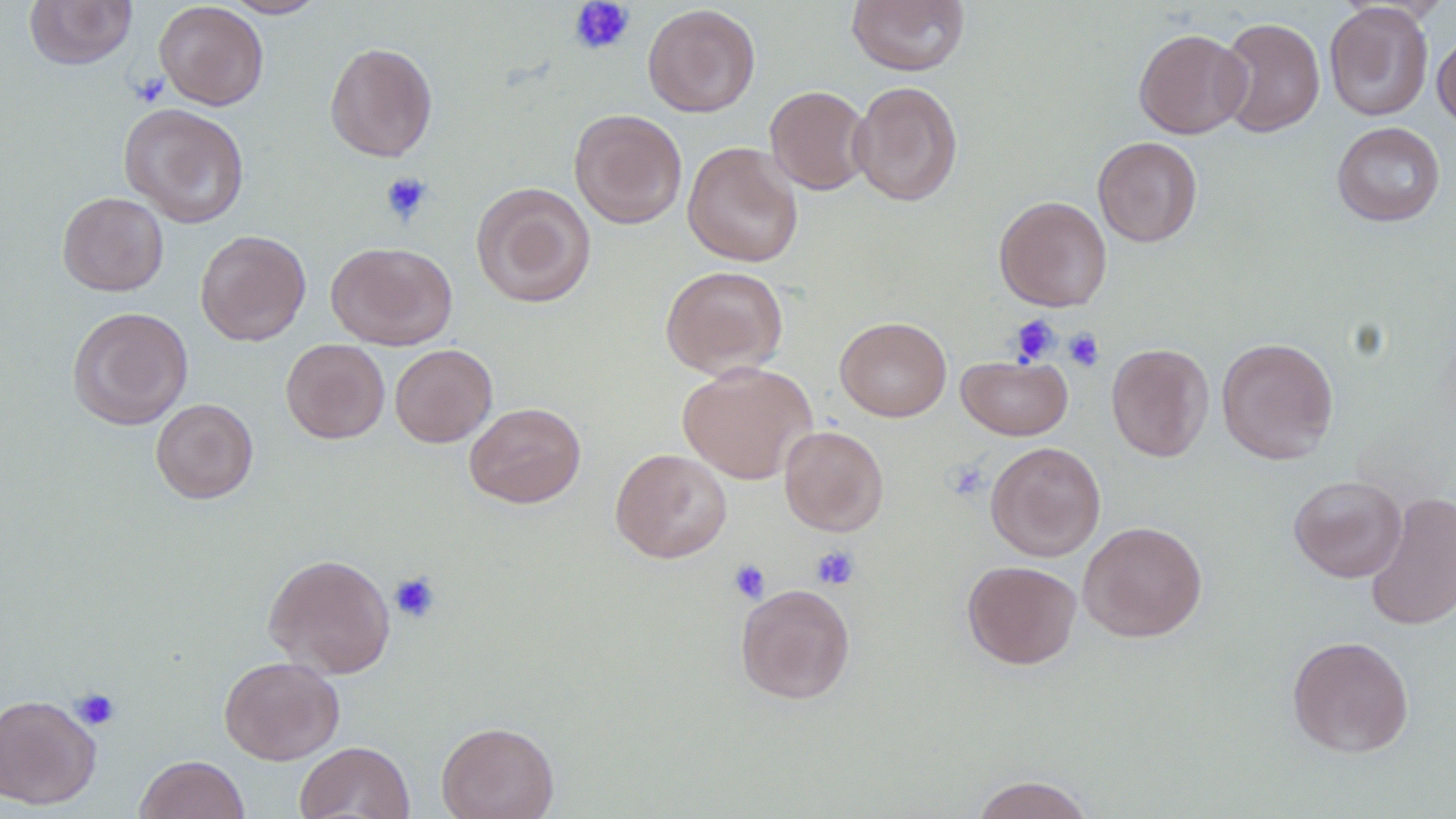 Approximate bounding boxes as named x1/y1/x2/y2 corners in pixels. Uninfected red blood cell locations: (x1=25, y1=0, x2=137, y2=70), (x1=223, y1=0, x2=328, y2=18), (x1=154, y1=1, x2=269, y2=110), (x1=847, y1=1, x2=970, y2=76), (x1=1324, y1=2, x2=1434, y2=121), (x1=642, y1=3, x2=761, y2=117), (x1=1217, y1=16, x2=1325, y2=137), (x1=1134, y1=28, x2=1252, y2=139), (x1=1432, y1=30, x2=1456, y2=133), (x1=324, y1=41, x2=438, y2=162), (x1=849, y1=80, x2=963, y2=206), (x1=765, y1=85, x2=873, y2=195), (x1=119, y1=103, x2=250, y2=228), (x1=569, y1=108, x2=687, y2=229), (x1=1331, y1=121, x2=1446, y2=227), (x1=1092, y1=136, x2=1203, y2=247), (x1=682, y1=141, x2=803, y2=268), (x1=471, y1=182, x2=597, y2=308), (x1=57, y1=191, x2=169, y2=296), (x1=994, y1=195, x2=1112, y2=312), (x1=195, y1=229, x2=311, y2=345), (x1=326, y1=241, x2=457, y2=350), (x1=660, y1=265, x2=789, y2=379), (x1=67, y1=306, x2=193, y2=430), (x1=835, y1=316, x2=952, y2=421), (x1=1216, y1=337, x2=1339, y2=464), (x1=281, y1=339, x2=390, y2=444), (x1=1106, y1=342, x2=1213, y2=461), (x1=390, y1=344, x2=497, y2=447), (x1=957, y1=355, x2=1073, y2=441), (x1=677, y1=361, x2=816, y2=484), (x1=150, y1=398, x2=259, y2=504), (x1=464, y1=402, x2=586, y2=508), (x1=779, y1=425, x2=889, y2=536), (x1=985, y1=442, x2=1106, y2=562), (x1=611, y1=448, x2=732, y2=563), (x1=1288, y1=475, x2=1407, y2=583), (x1=1364, y1=491, x2=1456, y2=631), (x1=1078, y1=521, x2=1207, y2=642), (x1=262, y1=553, x2=396, y2=678), (x1=962, y1=560, x2=1081, y2=669), (x1=735, y1=583, x2=856, y2=704), (x1=1287, y1=635, x2=1415, y2=758), (x1=218, y1=656, x2=345, y2=765), (x1=0, y1=694, x2=102, y2=810), (x1=436, y1=721, x2=559, y2=819), (x1=296, y1=741, x2=414, y2=819), (x1=134, y1=754, x2=250, y2=819), (x1=970, y1=774, x2=1094, y2=819). Platelet locations: (x1=568, y1=0, x2=635, y2=55), (x1=129, y1=71, x2=170, y2=107), (x1=380, y1=172, x2=434, y2=225), (x1=1010, y1=314, x2=1061, y2=365), (x1=1063, y1=328, x2=1105, y2=372), (x1=945, y1=460, x2=991, y2=500), (x1=810, y1=545, x2=861, y2=590), (x1=728, y1=559, x2=771, y2=604), (x1=389, y1=571, x2=441, y2=623), (x1=71, y1=687, x2=121, y2=730). Slide-level diagnosis: negative for blood parasites. Light microscopy. Thin blood smear. Captured at 1000x magnification. May-Grünwald-Giemsa-stained preparation. Image is 1456×819 pixels. One field of a larger specimen.